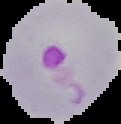

preparation: thin blood film
image_type: cell region segmented out of the field of view; surrounding area masked to black
image_size: 121×124 pixels
result: Plasmodium parasites detected